Locate every blood parasite and identify its species.
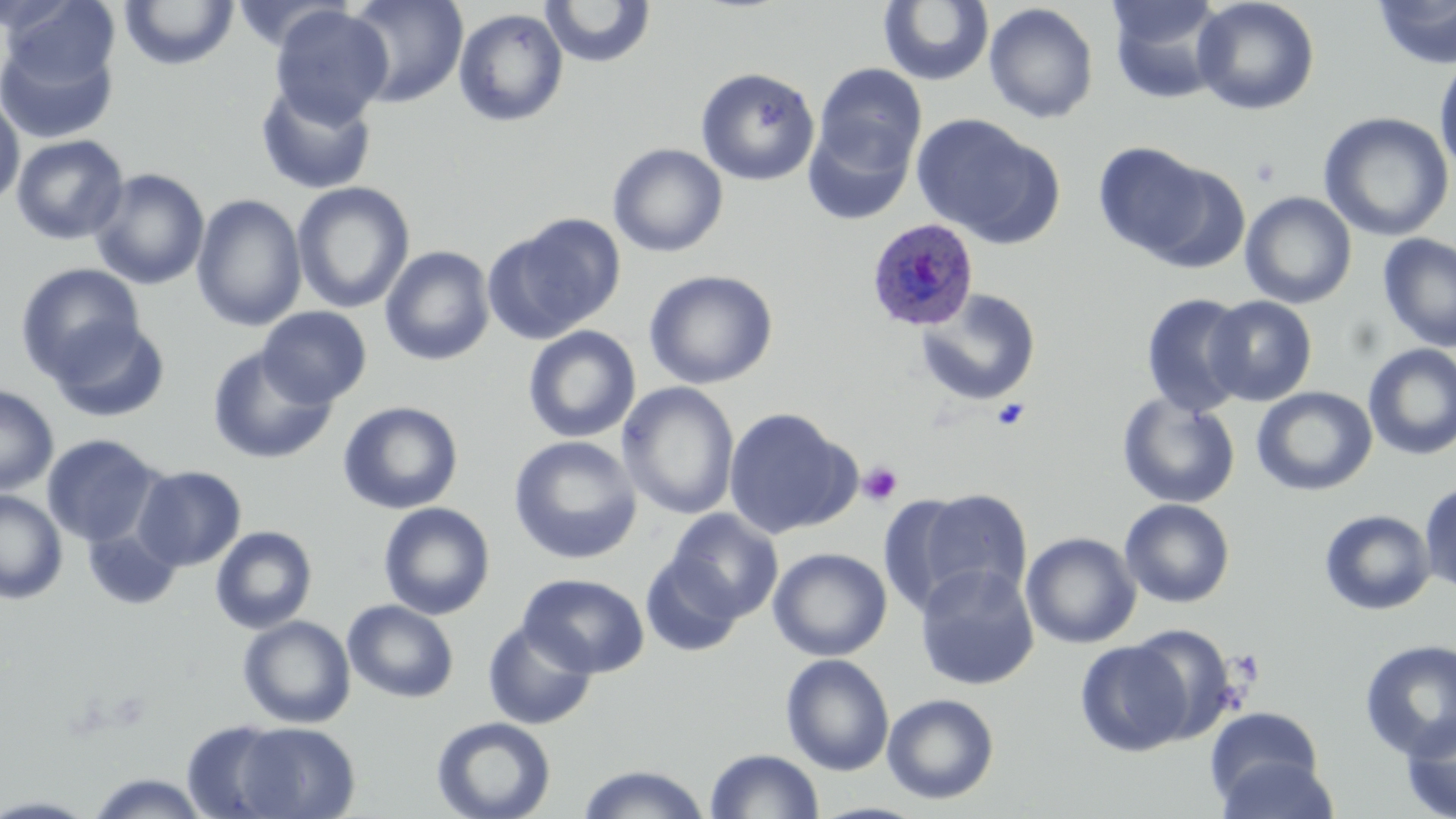

Approximate bounding boxes as [x1, y1, x2, y2] in pixels.
Plasmodium ovale-infected red blood cells: [866, 219, 980, 330].
No Plasmodium falciparum, Plasmodium malariae, Plasmodium vivax, Babesia divergens, or Trypanosoma brucei observed.

Summary:
  - Uninfected red blood cell locations: [3, 0, 120, 93], [1106, 0, 1229, 104], [1192, 0, 1320, 116], [1373, 0, 1456, 70], [118, 1, 240, 71], [346, 1, 468, 108], [539, 1, 657, 68], [878, 1, 995, 87], [984, 3, 1099, 124], [269, 5, 394, 126], [453, 8, 569, 128], [0, 29, 119, 144], [1434, 54, 1456, 180], [813, 63, 927, 176], [695, 67, 820, 186], [255, 80, 377, 195], [0, 94, 25, 211], [1318, 111, 1454, 242], [911, 113, 1059, 246], [803, 119, 916, 226], [11, 133, 129, 245], [1093, 142, 1211, 259], [607, 143, 728, 258], [1138, 160, 1251, 274], [89, 168, 210, 290], [292, 181, 414, 314], [1240, 191, 1357, 309], [191, 193, 307, 332], [485, 214, 625, 344], [1378, 232, 1456, 352], [379, 245, 495, 366], [15, 263, 146, 384], [643, 269, 779, 390], [914, 289, 1041, 406], [1140, 293, 1252, 416], [1204, 295, 1317, 406], [257, 306, 371, 408], [47, 315, 171, 423], [522, 325, 641, 443], [1362, 343, 1456, 460], [207, 345, 337, 465], [617, 382, 740, 520], [0, 385, 59, 496], [1251, 386, 1377, 496], [1117, 392, 1240, 508], [338, 400, 463, 515], [723, 407, 858, 539], [42, 433, 164, 548], [508, 435, 643, 565], [133, 465, 246, 571], [1419, 482, 1456, 597], [894, 486, 1036, 614], [0, 489, 68, 604], [1119, 499, 1235, 608], [378, 502, 495, 620], [666, 509, 783, 621], [1319, 509, 1436, 615], [82, 525, 182, 611], [210, 525, 317, 634], [1021, 532, 1141, 649], [768, 547, 892, 662], [640, 556, 744, 657], [914, 564, 1039, 691], [518, 573, 650, 677], [342, 599, 459, 703], [238, 615, 356, 728], [482, 620, 598, 729], [1126, 624, 1240, 744], [1075, 639, 1193, 757], [1359, 639, 1456, 761], [780, 653, 895, 776], [881, 693, 1000, 804], [1204, 706, 1326, 810], [1400, 713, 1456, 819], [431, 716, 556, 819], [182, 719, 298, 817], [229, 721, 361, 818], [704, 748, 824, 818], [1214, 752, 1338, 819], [576, 764, 712, 819], [85, 772, 211, 818], [0, 795, 98, 817]
  - Platelet locations: [1249, 155, 1282, 187], [990, 398, 1031, 432], [857, 461, 904, 507]
  - Slide-level diagnosis: Plasmodium ovale
  - Preparation: thin blood film
  - Modality: optical microscopy
  - Field of view: one of a larger specimen
  - Stain: May-Grünwald-Giemsa
  - Image size: 1456×819 pixels
  - Magnification: 1000x